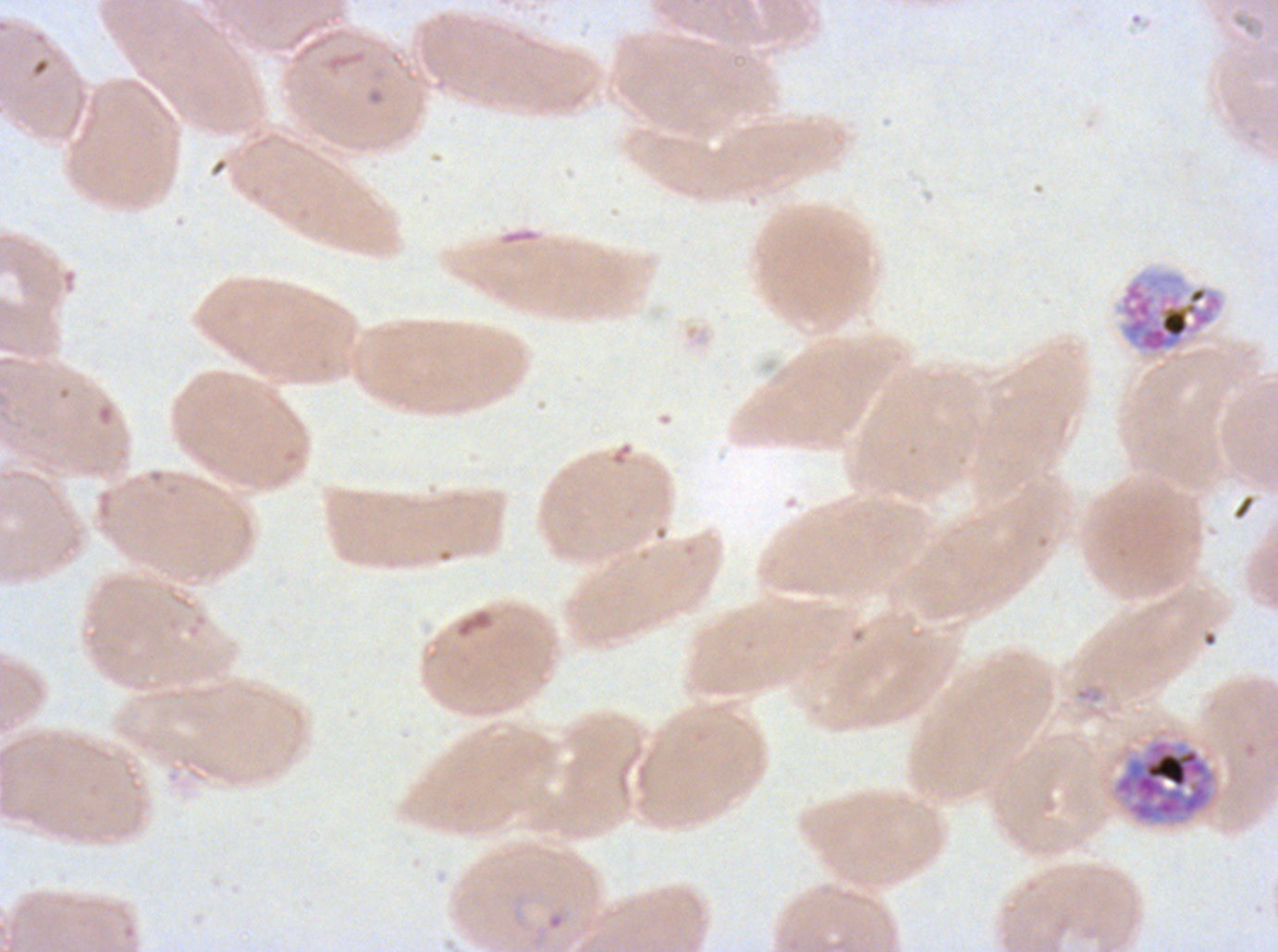 Approximate bounding boxes as (x1, y1, x2, y2) in pixels. Late schizont locations: (1113, 738, 1215, 823). Ring locations: (531, 908, 568, 949). Segmenter locations: (1117, 269, 1225, 358). Thin blood film. Ex-vivo Plasmodium falciparum culture from a patient in The Gambia, grown for 24 to 48 hours. Life-cycle stages observed: ring, late schizont, segmenter. One sub-image of a larger composite. Image is 1278×952 pixels. Giemsa stain.